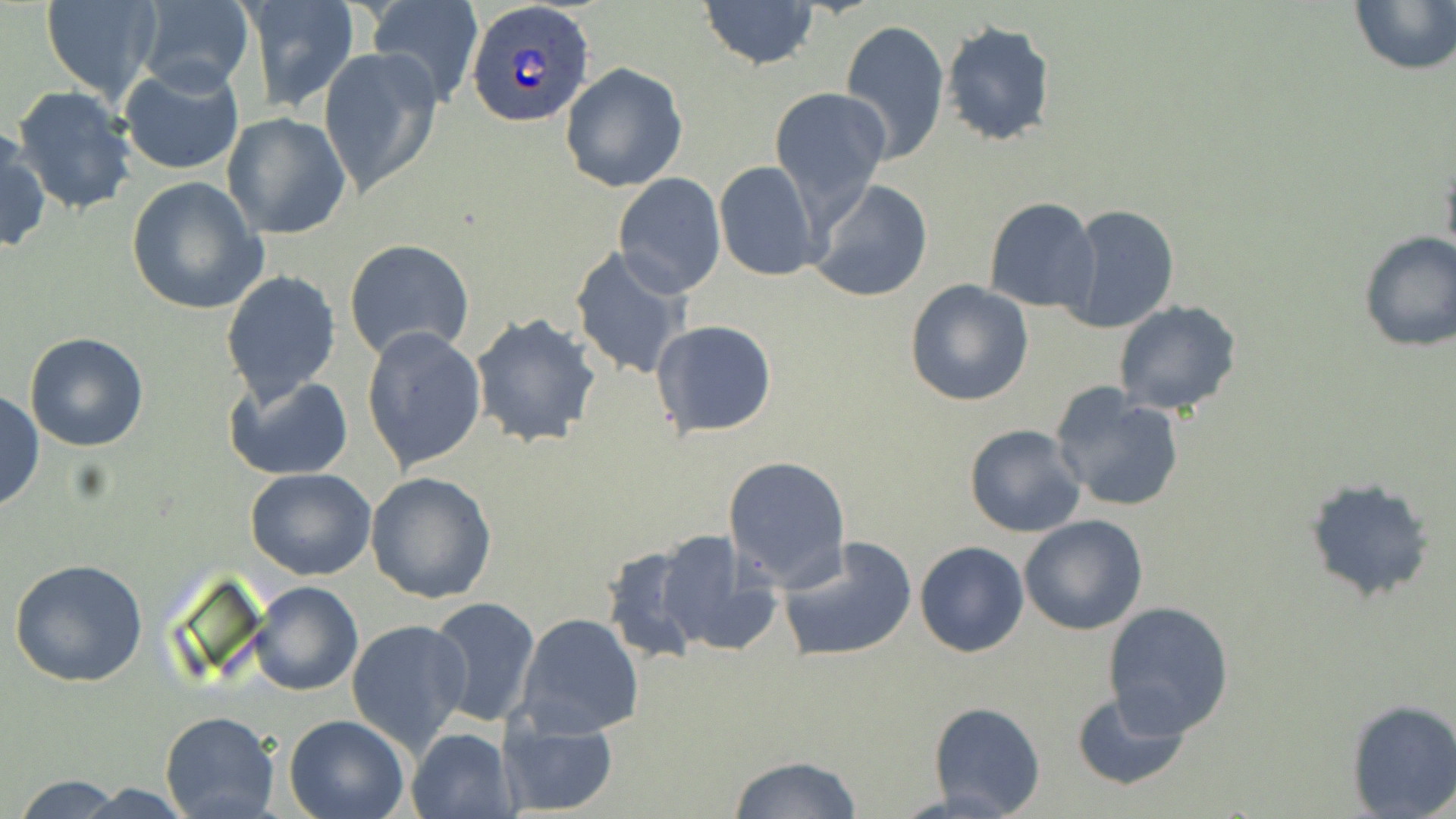
{
  "plasmodium_ovale_infected_red_blood_cell_locations": "approximate bounding boxes as [x1, y1, x2, y2] in pixels: [466, 4, 596, 127]",
  "slide_level_diagnosis": "Plasmodium ovale",
  "modality": "optical microscopy",
  "stain": "May-Grünwald-Giemsa",
  "magnification": "1000x",
  "uninfected_red_blood_cell_locations": "approximate bounding boxes as [x1, y1, x2, y2] in pixels: [41, 0, 162, 101], [366, 0, 484, 107], [698, 0, 819, 71], [1348, 0, 1455, 75], [236, 1, 358, 115], [129, 3, 255, 94], [841, 19, 950, 162], [941, 20, 1057, 146], [319, 47, 443, 199], [559, 62, 688, 193], [119, 63, 244, 175], [10, 85, 138, 216], [769, 88, 892, 218], [221, 113, 351, 240], [0, 131, 50, 254], [714, 160, 820, 281], [1441, 160, 1456, 265], [612, 173, 725, 296], [126, 177, 267, 314], [807, 180, 933, 303], [983, 196, 1101, 313], [1057, 204, 1180, 333], [1356, 229, 1456, 352], [345, 238, 476, 362], [570, 245, 693, 382], [222, 271, 342, 405], [905, 278, 1034, 406], [1114, 301, 1243, 416], [470, 311, 601, 449], [649, 320, 779, 439], [362, 327, 487, 474], [24, 331, 150, 451], [223, 373, 354, 481], [1051, 383, 1187, 514], [1, 391, 44, 512], [963, 423, 1086, 538], [723, 455, 852, 589], [245, 466, 376, 581], [366, 471, 498, 605], [1303, 477, 1435, 604], [1019, 515, 1149, 636], [644, 527, 781, 658], [777, 535, 917, 662], [914, 540, 1029, 657], [9, 557, 151, 687], [249, 580, 362, 695], [425, 597, 543, 726], [1102, 601, 1234, 738], [515, 613, 643, 740], [346, 620, 473, 753], [1069, 689, 1191, 792], [1345, 699, 1456, 818], [927, 701, 1046, 817], [160, 711, 279, 819], [284, 714, 411, 819], [494, 715, 618, 817], [407, 728, 517, 819], [727, 754, 862, 817], [9, 776, 132, 818]",
  "field_of_view": "one of a larger specimen",
  "preparation": "thin blood smear",
  "image_size": "1456×819 pixels"
}